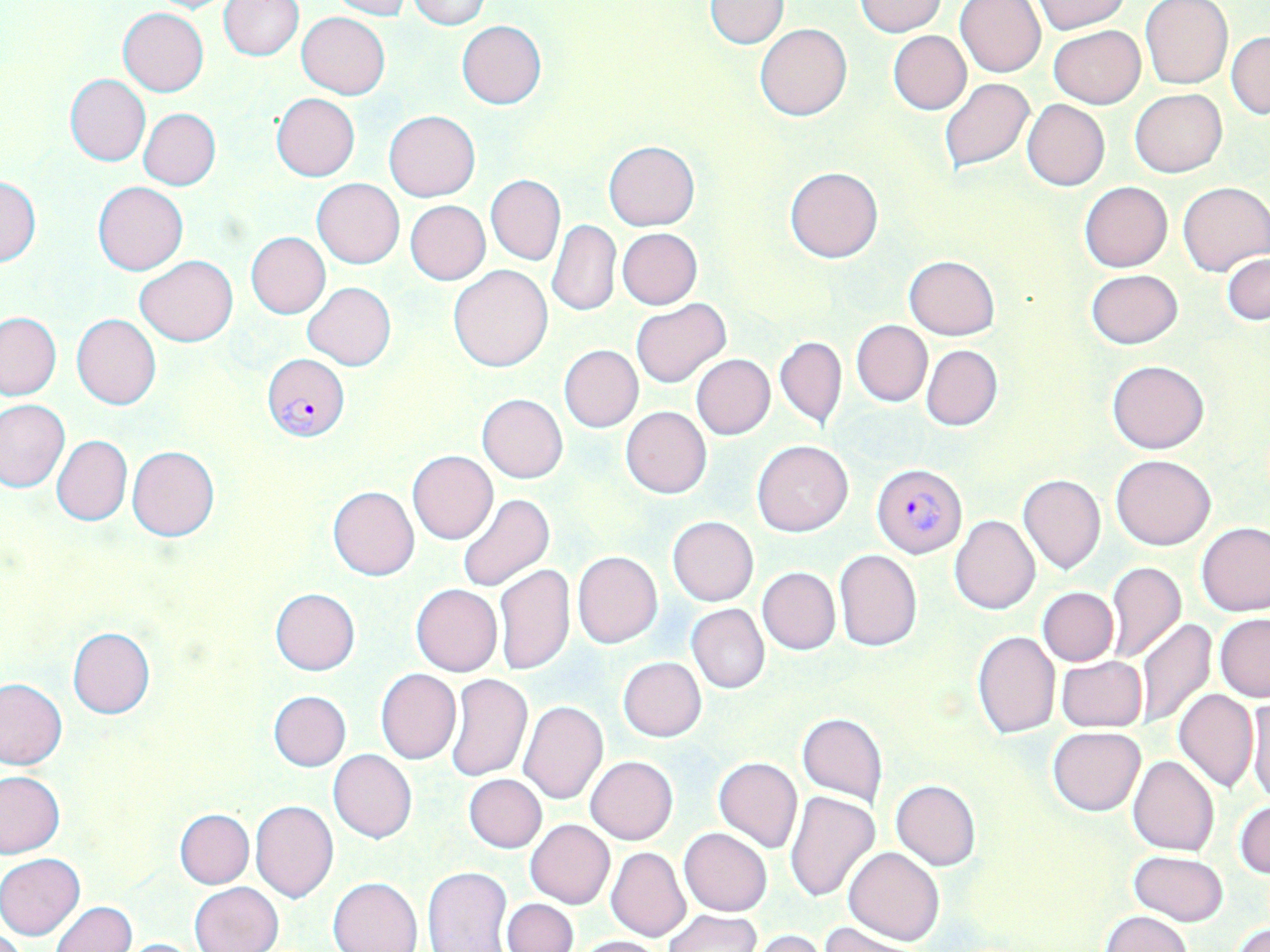

{
  "slide_level_diagnosis": "Plasmodium falciparum",
  "uninfected_red_blood_cell_locations": "approximate bounding boxes as (x1,y1)-(x2,y2) corner pairs in pixels: (139,0)-(239,13), (328,0)-(412,19), (407,0)-(492,27), (954,0)-(1047,77), (1031,0)-(1130,34), (218,1)-(303,60), (704,1)-(789,49), (856,1)-(948,36), (1140,1)-(1232,89), (118,8)-(208,95), (296,12)-(391,99), (456,21)-(547,108), (754,23)-(852,121), (1047,26)-(1145,109), (888,29)-(972,115), (1227,31)-(1270,119), (64,75)-(150,166), (939,79)-(1035,173), (1129,88)-(1227,177), (271,94)-(360,181), (1022,99)-(1109,191), (137,108)-(220,190), (384,111)-(480,202), (603,141)-(701,231), (785,166)-(883,263), (0,175)-(41,266), (487,175)-(565,265), (312,179)-(405,269), (92,180)-(188,275), (1080,181)-(1172,272), (1178,181)-(1270,276), (405,201)-(491,285), (547,219)-(621,318), (618,228)-(702,309), (246,232)-(331,318), (1222,252)-(1269,324), (904,255)-(1000,340), (134,256)-(239,345), (448,265)-(553,372), (1086,269)-(1183,349), (302,283)-(396,370), (630,299)-(730,388), (0,311)-(62,401), (71,313)-(161,410), (851,320)-(932,406), (775,336)-(846,428), (921,344)-(1002,430), (559,345)-(643,433), (692,354)-(775,439), (1107,360)-(1210,454), (477,394)-(567,483), (0,399)-(69,491), (620,406)-(712,498), (51,434)-(131,526), (752,440)-(854,536), (128,446)-(219,541), (408,450)-(497,543), (1110,454)-(1217,550), (1017,474)-(1106,575), (327,486)-(420,581), (456,492)-(554,592), (484,508)-(573,641), (950,514)-(1039,615), (668,516)-(758,605), (1196,522)-(1270,616), (834,549)-(922,652), (572,551)-(662,648), (1106,560)-(1187,665), (494,563)-(575,676), (756,566)-(840,654), (411,584)-(501,676), (1037,587)-(1118,666), (270,588)-(360,675), (686,604)-(769,693), (1215,614)-(1270,702), (1135,618)-(1216,731), (66,626)-(156,719), (971,631)-(1061,739), (1055,655)-(1147,732), (617,657)-(707,741), (375,669)-(461,764), (445,674)-(532,781), (0,678)-(66,769), (1173,688)-(1258,792), (268,690)-(351,770), (1246,694)-(1270,808), (518,700)-(608,805), (797,713)-(888,807), (1047,726)-(1147,817), (329,750)-(416,844), (586,755)-(678,845), (1128,756)-(1219,856), (714,757)-(802,853), (0,771)-(65,858), (464,775)-(546,853), (891,780)-(980,870), (785,790)-(879,902), (1234,799)-(1270,879), (251,800)-(337,903), (175,808)-(254,888), (525,819)-(614,908), (679,828)-(773,916), (605,846)-(690,941), (844,847)-(945,946), (1130,851)-(1228,924), (0,853)-(85,940), (423,866)-(513,951), (328,877)-(422,952), (190,881)-(283,952), (502,897)-(578,951), (50,901)-(136,952), (663,909)-(761,952), (1102,911)-(1192,952), (822,921)-(912,952), (1231,922)-(1269,952), (748,930)-(828,952), (576,935)-(666,952), (115,938)-(206,951)",
  "stain": "May-Grünwald-Giemsa",
  "magnification": "1000x",
  "field_of_view": "single",
  "modality": "light microscopy",
  "preparation": "thin blood film",
  "image_size": "1270×952 pixels",
  "plasmodium_falciparum_infected_red_blood_cell_locations": "approximate bounding boxes as (x1,y1)-(x2,y2) corner pairs in pixels: (262,353)-(349,443), (871,464)-(967,558)"
}